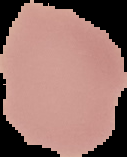
image size = 127×157 pixels
result = negative for Plasmodium parasites
preparation = thin blood film
image type = segmented cell region with the area outside set to black